Identify the parasite.
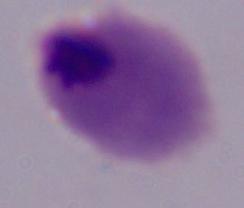
This is a trichomonad.

1000x magnification. Photomicrograph.